Locate every malaria parasite and every leukocyte.
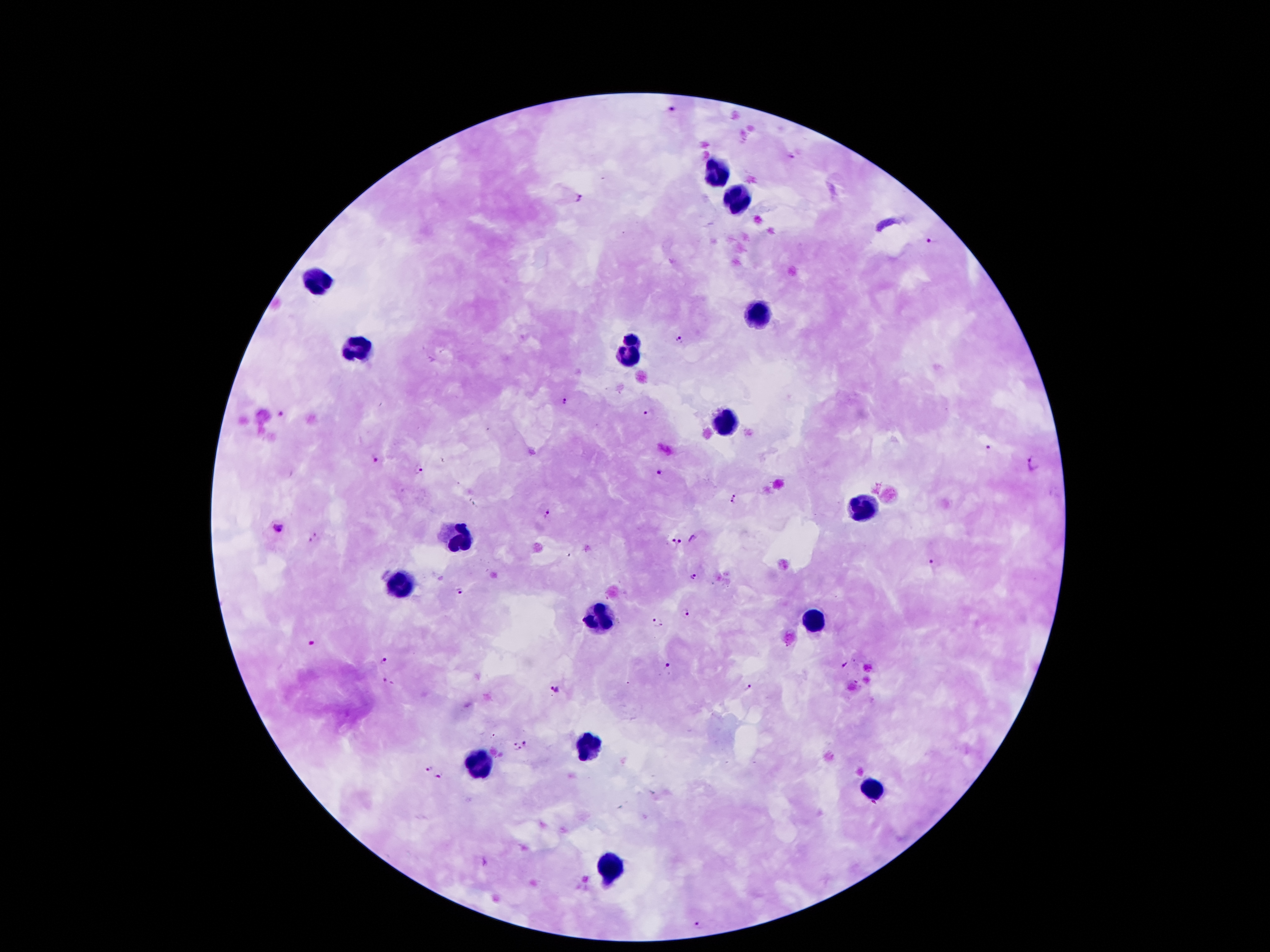
Approximate object centers, in pixels from the top-left corner.
Malaria parasites: (x=673, y=108), (x=792, y=155), (x=579, y=197), (x=930, y=242), (x=679, y=338), (x=564, y=401), (x=280, y=412), (x=650, y=415), (x=986, y=446), (x=1035, y=459), (x=374, y=460), (x=419, y=470), (x=660, y=470), (x=736, y=496), (x=548, y=515), (x=277, y=527), (x=314, y=538), (x=694, y=538), (x=676, y=543), (x=935, y=565), (x=692, y=573), (x=461, y=593), (x=687, y=611), (x=660, y=622), (x=311, y=643), (x=384, y=659), (x=668, y=665), (x=844, y=665), (x=388, y=682), (x=749, y=688), (x=556, y=690), (x=527, y=742), (x=517, y=748), (x=427, y=765), (x=439, y=776), (x=700, y=924).
Leukocytes: (x=716, y=175), (x=738, y=203), (x=320, y=283), (x=756, y=314), (x=632, y=338), (x=358, y=351), (x=630, y=356), (x=727, y=422), (x=860, y=508), (x=459, y=537), (x=397, y=584), (x=599, y=619), (x=813, y=621), (x=590, y=745), (x=477, y=765), (x=877, y=789), (x=607, y=862).

Summary:
  - Stain: Giemsa
  - Preparation: thick peripheral-blood smear
  - Patient malaria status: infected with Plasmodium falciparum
  - Field of view: single
  - Magnification: 100x
  - Image size: 1270×952 pixels
  - Capture: smartphone camera through the microscope eyepiece